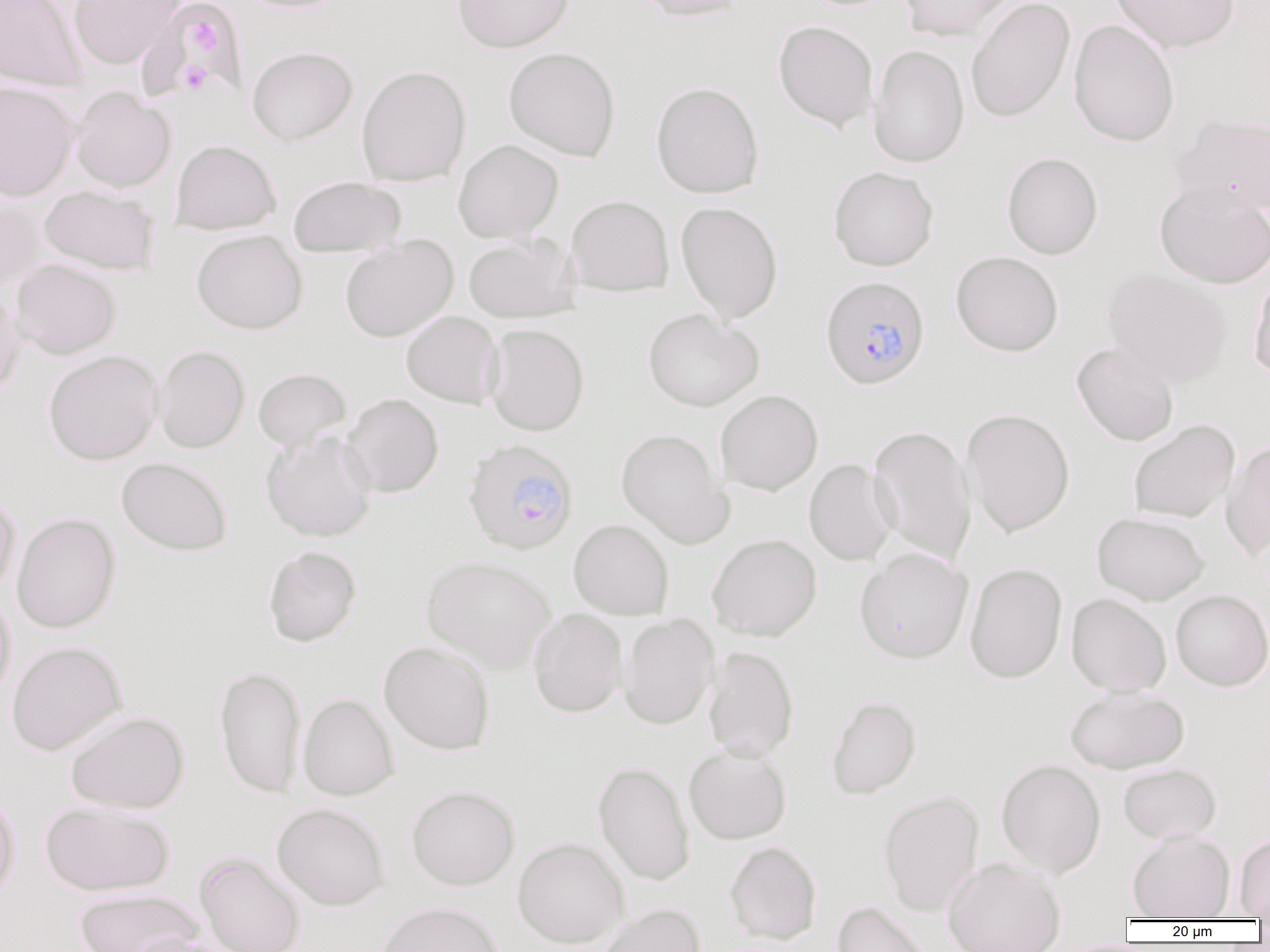

Plasmodium falciparum-infected red blood cell locations (subset) = approximate bounding boxes as (x1, y1, x2, y2) in pixels: (819, 275, 931, 390), (459, 445, 576, 563)
slide-level diagnosis = Plasmodium falciparum
platelet locations = approximate bounding boxes as (x1, y1, x2, y2) in pixels: (188, 17, 221, 55), (178, 60, 211, 95)
magnification = 1000x
uninfected red blood cell locations (subset) = approximate bounding boxes as (x1, y1, x2, y2) in pixels: (0, 0, 86, 92), (68, 0, 185, 69), (234, 0, 354, 13), (453, 0, 574, 53), (631, 0, 750, 22), (898, 0, 1015, 42), (965, 0, 1075, 123), (1109, 0, 1240, 52), (139, 1, 246, 100), (1068, 19, 1180, 147), (773, 20, 879, 132), (868, 44, 969, 168), (247, 46, 358, 146), (503, 47, 621, 162), (356, 64, 471, 187), (0, 81, 79, 201), (651, 81, 764, 199), (70, 86, 176, 192), (1170, 112, 1270, 215), (170, 139, 281, 235), (453, 139, 563, 242), (1001, 152, 1103, 259), (828, 166, 939, 271), (288, 176, 406, 257), (1154, 180, 1270, 289), (39, 185, 159, 275), (0, 193, 48, 289), (565, 195, 675, 297), (675, 201, 783, 323), (192, 229, 308, 334), (463, 233, 579, 323), (340, 235, 459, 342), (950, 251, 1063, 356), (10, 259, 122, 359), (1102, 268, 1231, 387), (1249, 270, 1270, 380), (0, 284, 24, 396), (643, 308, 764, 412), (401, 310, 503, 408), (484, 323, 590, 436), (1072, 343, 1179, 447), (153, 345, 250, 453), (43, 350, 162, 465), (253, 368, 352, 450), (715, 390, 823, 496), (341, 393, 444, 498), (961, 407, 1076, 538), (1128, 419, 1240, 523), (868, 424, 977, 565), (616, 428, 734, 549), (261, 431, 378, 542), (1220, 440, 1270, 561), (116, 457, 233, 556), (803, 458, 899, 566), (0, 493, 20, 597), (11, 512, 121, 634), (1092, 512, 1210, 605), (568, 519, 674, 620), (707, 533, 822, 641), (263, 546, 362, 647), (854, 548, 973, 663), (421, 555, 556, 673), (963, 562, 1068, 684), (0, 589, 15, 706), (1170, 589, 1270, 690), (1066, 593, 1171, 696), (528, 608, 627, 718), (617, 614, 719, 730), (378, 640, 495, 755), (6, 641, 127, 755), (703, 645, 799, 761), (214, 665, 306, 799), (1065, 686, 1189, 774), (297, 693, 399, 801), (826, 696, 922, 799), (64, 710, 190, 814), (683, 744, 792, 845), (996, 759, 1106, 877), (593, 761, 695, 886), (1117, 763, 1221, 845), (406, 785, 520, 891), (0, 788, 21, 903), (878, 790, 984, 916), (40, 801, 175, 896), (272, 803, 391, 910), (1127, 831, 1235, 919), (1234, 834, 1270, 919), (512, 837, 629, 948), (724, 841, 822, 944), (942, 857, 1067, 952), (74, 888, 202, 952), (375, 901, 503, 952), (832, 901, 936, 952), (597, 903, 705, 952), (122, 933, 237, 952)
field of view = single
modality = optical microscopy
image size = 1270×952 pixels
preparation = thin blood film